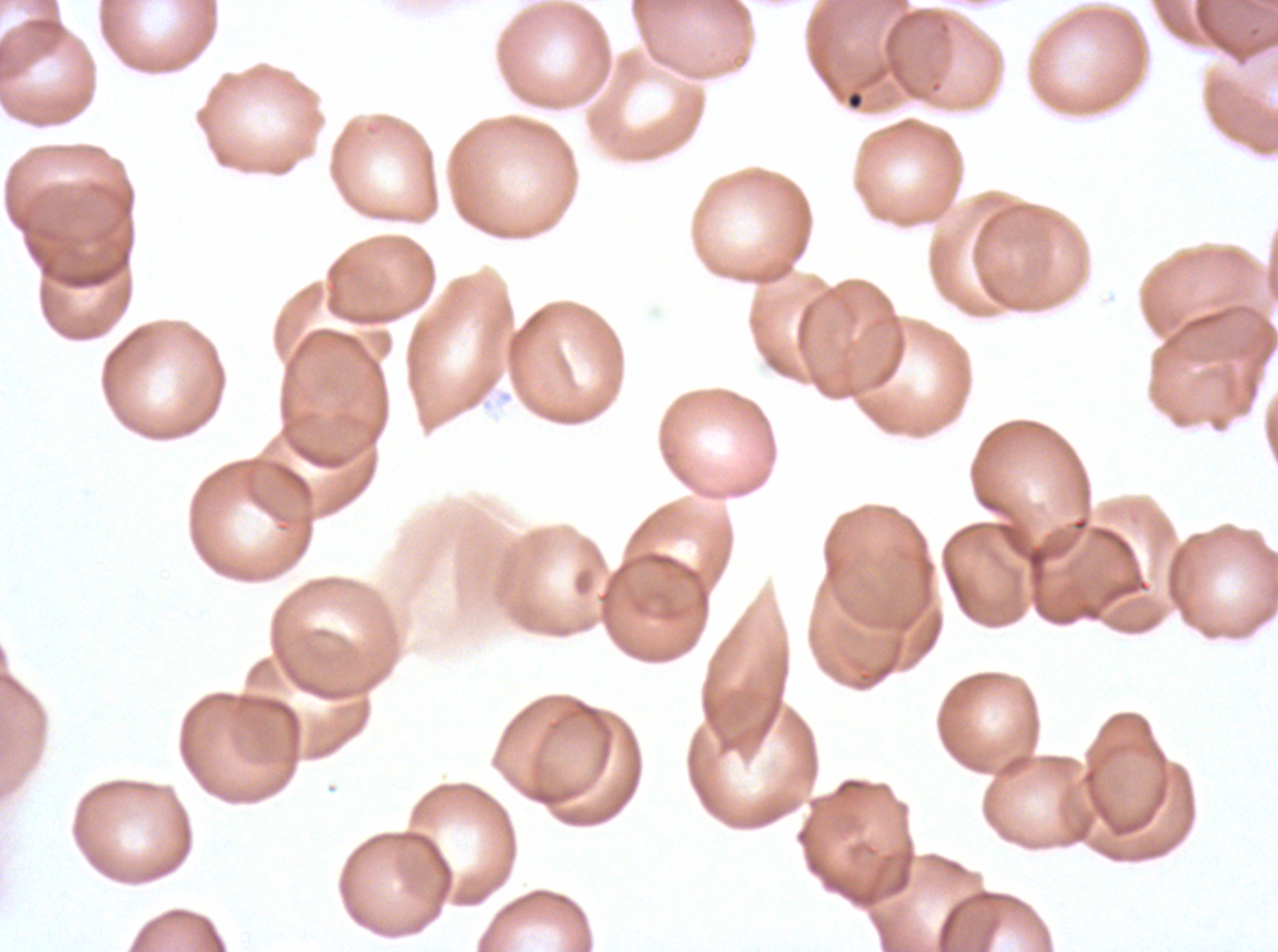

Approximate bounding boxes as [x1, y1, x2, y2] in pixels.
Summary:
  - Debris locations: [846, 91, 864, 110]
  - Preparation: thin blood film
  - Stain: Giemsa
  - Specimen: Plasmodium falciparum cultured ex vivo for 24 to 48 hours, from a patient in The Gambia
  - Image size: 1278×952 pixels
  - Field of view: one sub-image of a larger composite